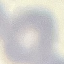

malaria status = uninfected
preparation = thin smear
stain = Giemsa
image type = cell patch, automatically extracted from a larger field of view and resized to 64 × 64 pixels
capture = smartphone through the microscope eyepiece